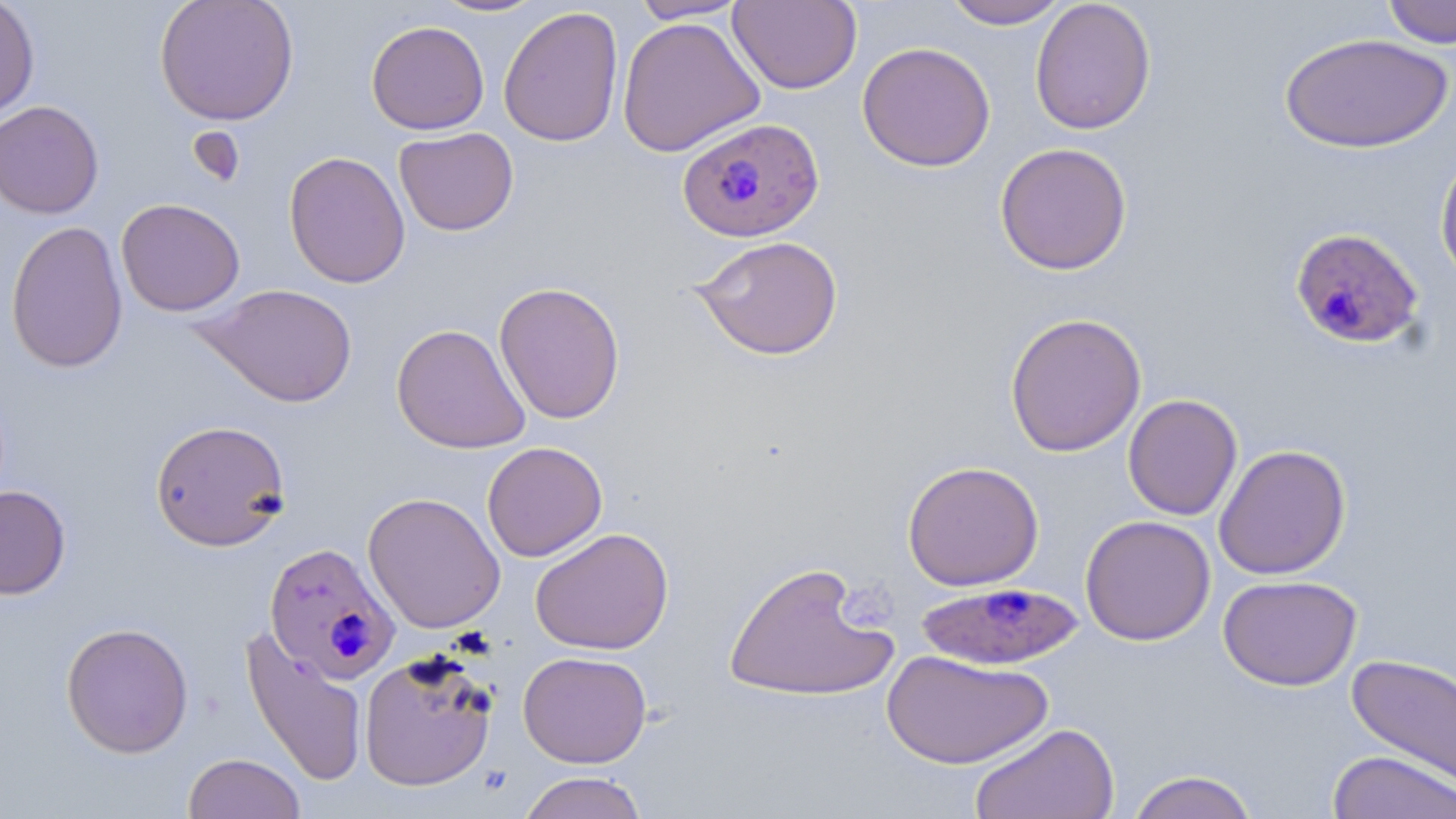
Summary:
  - Coordinate format: approximate bounding boxes as (x1, y1, x2, y2) in pixels
  - Uninfected red blood cell locations: (0, 0, 40, 122), (154, 0, 299, 125), (429, 0, 548, 18), (631, 0, 751, 23), (728, 0, 862, 94), (942, 0, 1070, 29), (1030, 0, 1156, 135), (1381, 0, 1456, 49), (498, 6, 624, 147), (617, 16, 766, 157), (366, 20, 489, 135), (1278, 31, 1453, 154), (857, 41, 996, 172), (0, 100, 104, 219), (394, 127, 519, 236), (994, 142, 1133, 275), (1434, 150, 1456, 286), (283, 151, 411, 289), (115, 197, 245, 317), (5, 220, 129, 374), (691, 235, 844, 360), (494, 281, 625, 424), (197, 283, 358, 407), (1004, 312, 1147, 457), (391, 323, 530, 454), (1122, 394, 1243, 520), (149, 419, 291, 552), (482, 442, 608, 562), (1213, 443, 1351, 580), (902, 460, 1044, 591), (0, 485, 71, 599), (362, 491, 505, 633), (1079, 515, 1216, 646), (530, 527, 674, 655), (722, 561, 897, 704), (1218, 574, 1362, 691), (60, 621, 194, 758), (241, 627, 368, 788), (881, 648, 1053, 770), (358, 649, 498, 792), (518, 650, 652, 768), (1346, 651, 1456, 796), (970, 722, 1119, 819), (1327, 750, 1455, 819), (183, 752, 306, 818), (1126, 769, 1261, 819), (517, 771, 649, 819)
  - Plasmodium falciparum-infected red blood cell locations: (676, 116, 824, 242), (1290, 226, 1425, 351), (263, 541, 401, 684), (916, 580, 1084, 670)
  - Slide-level diagnosis: Plasmodium falciparum
  - Preparation: thin blood smear
  - Image size: 1456×819 pixels
  - Field of view: single
  - Modality: optical microscopy
  - Stain: May-Grünwald-Giemsa
  - Magnification: 1000x